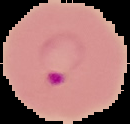 From a thin blood film. Malaria status: parasitized. Image is 130×124 pixels. Cell region segmented out of the field of view; the surrounding area is masked to black.